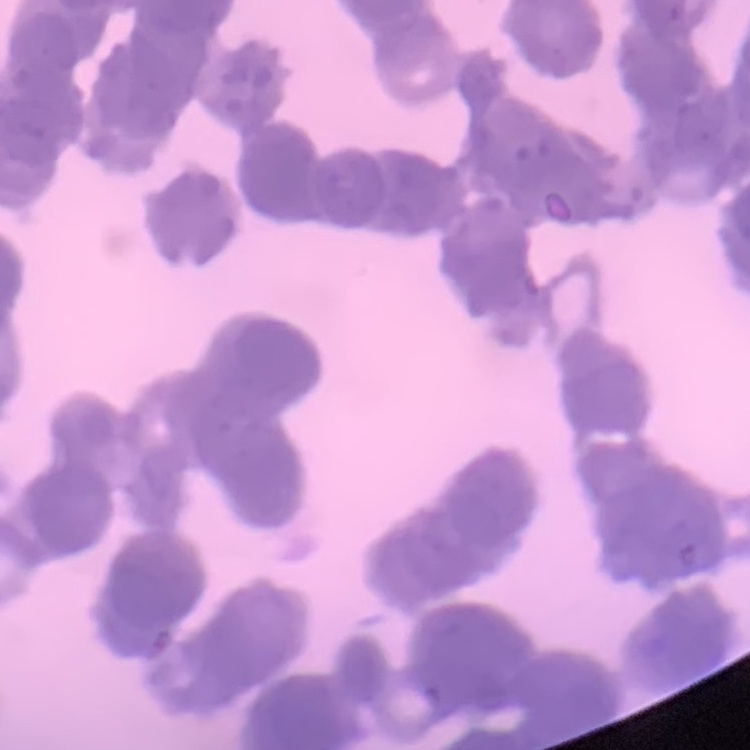

red_blood_cell_morphology: rouleaux formation
image_type: one tile cut from a larger photomicrograph
preparation: thin blood smear
stain: Field's or Giemsa